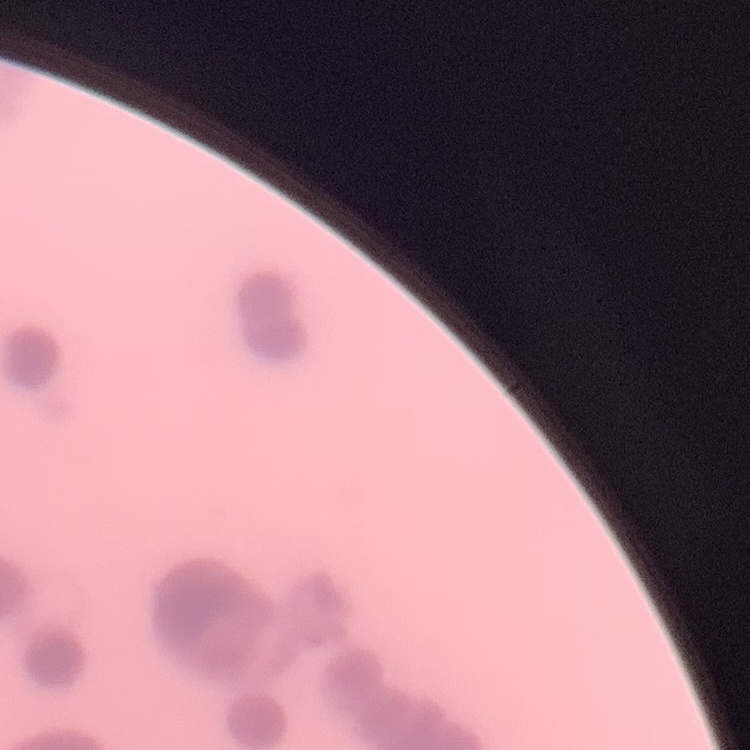

The erythrocytes exhibit rouleaux formation. Thin blood smear. Field's or Giemsa stain. Square crop of a larger photomicrograph.